Report the malaria status of this cell.
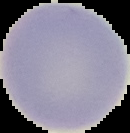

It is uninfected.

preparation = thin blood film
image type = segmented cell region on a black background
image size = 130×133 pixels